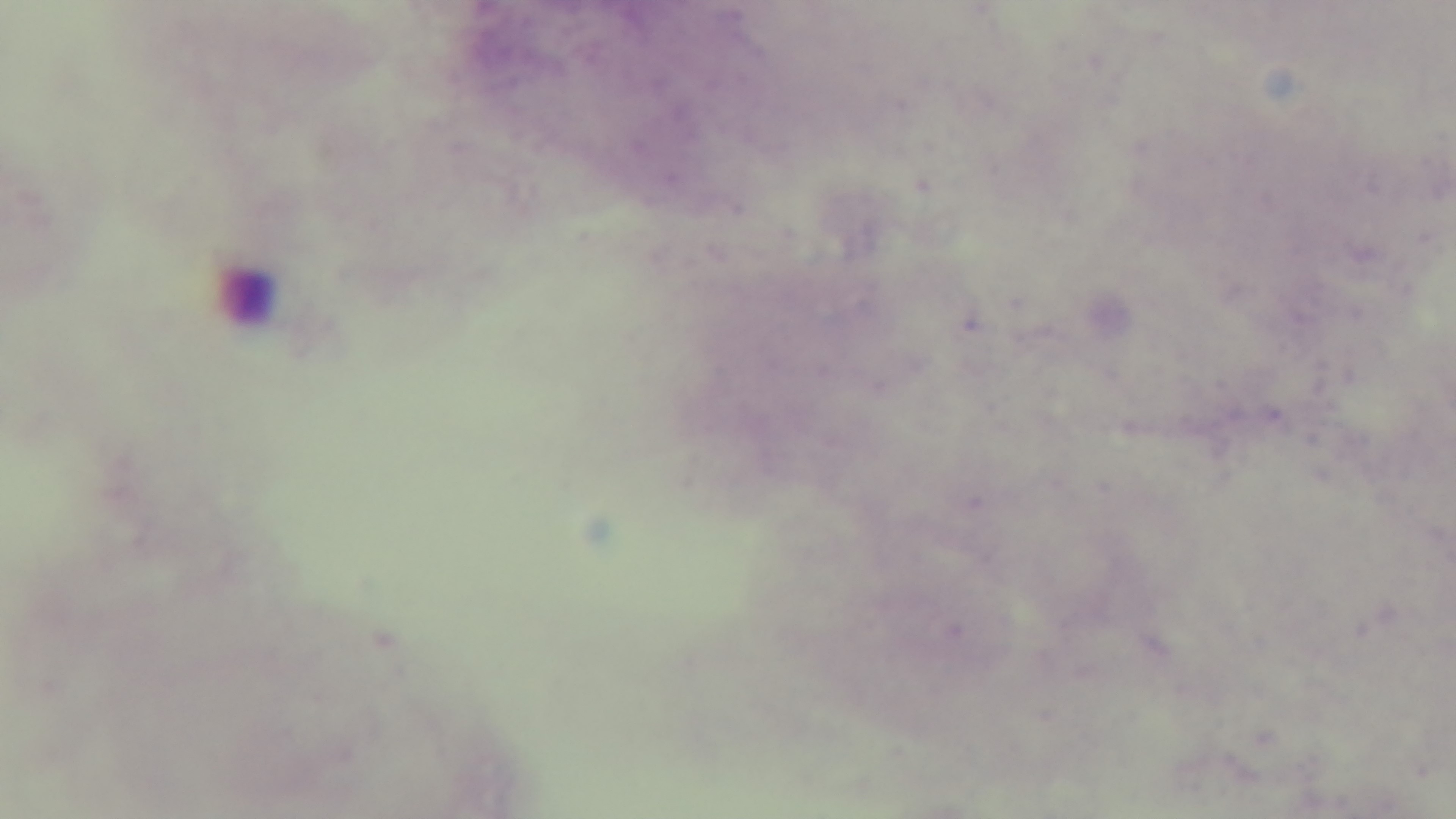
Malaria status: negative. Mounted 4K digital camera. One field from the slide. Oil-immersion objective, 100x. Photomicrograph. Preparation: thick smear. Giemsa stain.